Assess this cell for malaria.
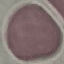
It is uninfected.

image_type: automatically extracted cell patch, resized to 64 × 64 pixels
stain: Giemsa
capture: smartphone through the microscope eyepiece
preparation: thin blood smear